Locate and identify every blood parasite.
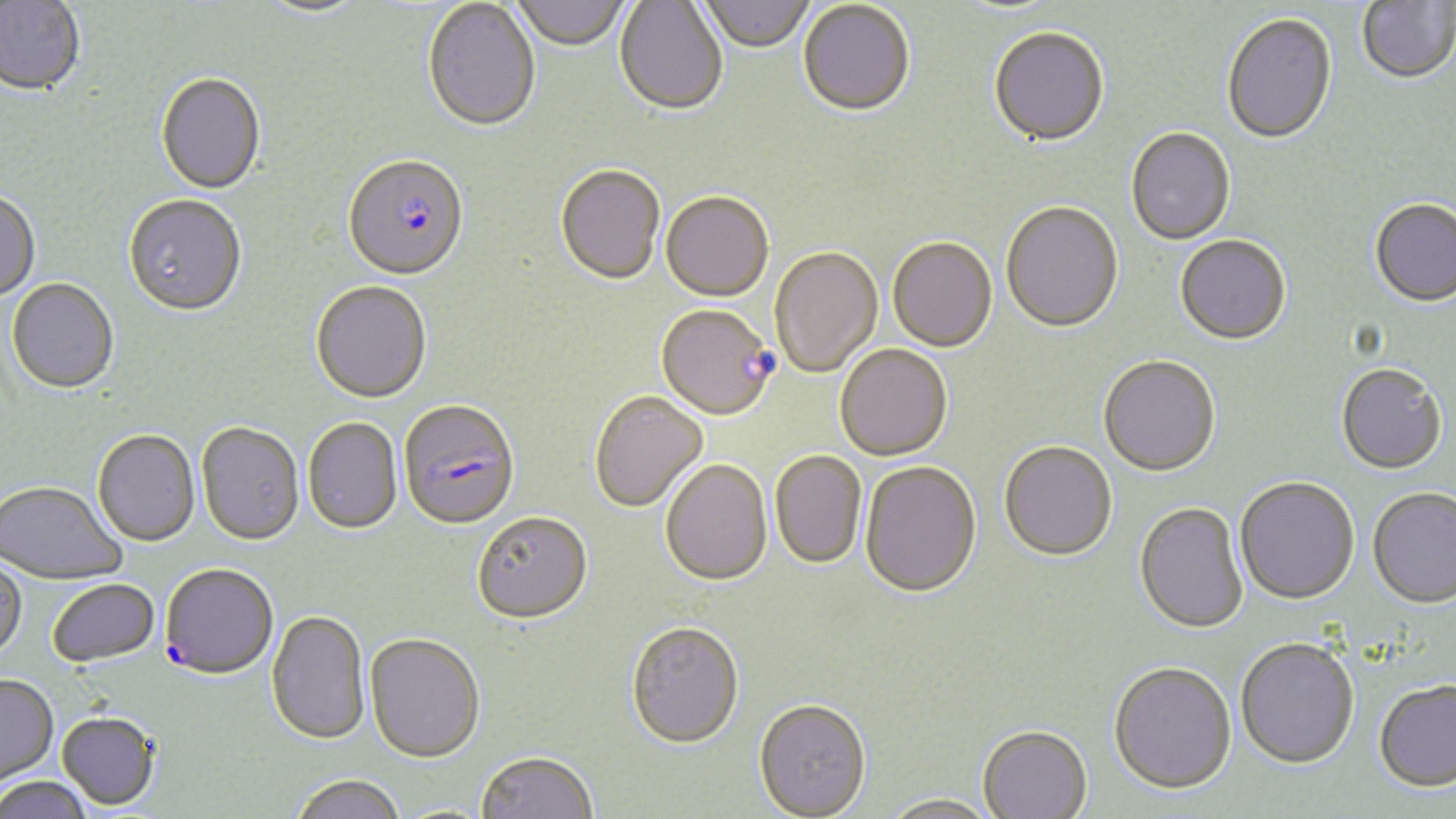

Approximate bounding boxes as [x1, y1, x2, y2] in pixels.
Plasmodium falciparum-infected red blood cells: [343, 158, 470, 284], [657, 305, 777, 421], [398, 401, 520, 532], [160, 565, 278, 681].
No Plasmodium ovale, Plasmodium malariae, Plasmodium vivax, Babesia divergens, or Trypanosoma brucei observed.

{
  "slide_level_diagnosis": "Plasmodium falciparum",
  "field_of_view": "single",
  "uninfected_red_blood_cell_locations": "approximate bounding boxes as [x1, y1, x2, y2] in pixels: [512, 0, 630, 52], [699, 0, 815, 54], [0, 1, 87, 98], [255, 1, 371, 21], [422, 1, 541, 134], [615, 1, 728, 116], [1357, 1, 1456, 85], [798, 2, 915, 119], [1221, 15, 1337, 147], [989, 29, 1109, 149], [155, 74, 266, 196], [1126, 129, 1235, 246], [554, 166, 665, 287], [0, 190, 41, 302], [661, 193, 774, 303], [123, 196, 247, 317], [1369, 199, 1456, 309], [1001, 203, 1124, 335], [1175, 236, 1291, 347], [887, 238, 997, 354], [770, 247, 882, 378], [6, 279, 119, 395], [311, 283, 433, 405], [835, 345, 953, 462], [1098, 357, 1221, 478], [1336, 364, 1447, 475], [589, 391, 709, 513], [302, 417, 404, 535], [196, 423, 304, 547], [92, 430, 200, 548], [999, 443, 1117, 563], [770, 451, 866, 570], [661, 460, 772, 586], [860, 462, 982, 600], [1235, 478, 1360, 606], [0, 481, 127, 585], [1367, 488, 1456, 610], [1134, 503, 1248, 636], [471, 514, 592, 626], [0, 557, 27, 664], [48, 579, 161, 669], [266, 610, 371, 747], [625, 622, 744, 749], [365, 634, 485, 764], [1236, 639, 1359, 770], [1108, 664, 1236, 797], [0, 675, 59, 790], [1373, 680, 1456, 794], [753, 698, 871, 818], [56, 713, 161, 811], [977, 727, 1093, 819], [476, 751, 598, 819], [290, 776, 407, 819], [0, 777, 95, 819], [879, 795, 1001, 819]",
  "preparation": "thin blood smear",
  "stain": "May-Grünwald-Giemsa",
  "modality": "optical microscopy",
  "image_size": "1456×819 pixels",
  "magnification": "1000x"
}